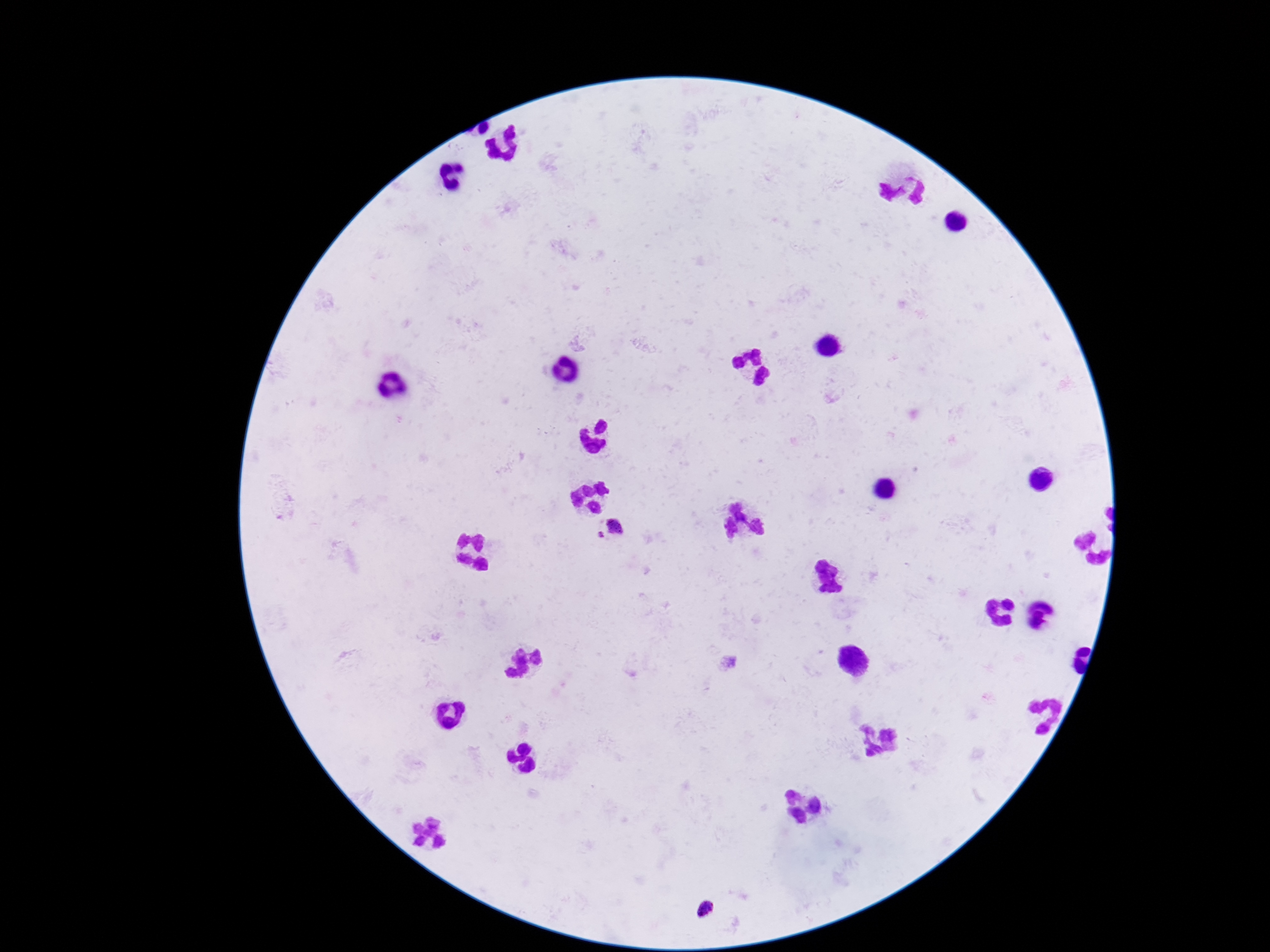

Approximate object centers, in pixels from the top-left corner. Plasmodium parasite locations: (x=613, y=530), (x=703, y=909). 100x magnification. Single field of view. Giemsa stain. Patient malaria status: infected. Image is 1270×952 pixels. Photographed through the microscope eyepiece with a smartphone camera. Thick blood film.